State which parasite is depicted.
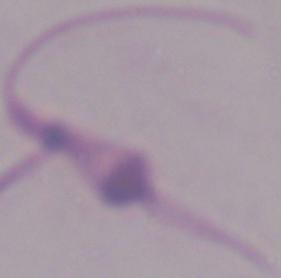

This is Leishmania.

Summary:
  - Modality: photomicrograph
  - Magnification: 1000x